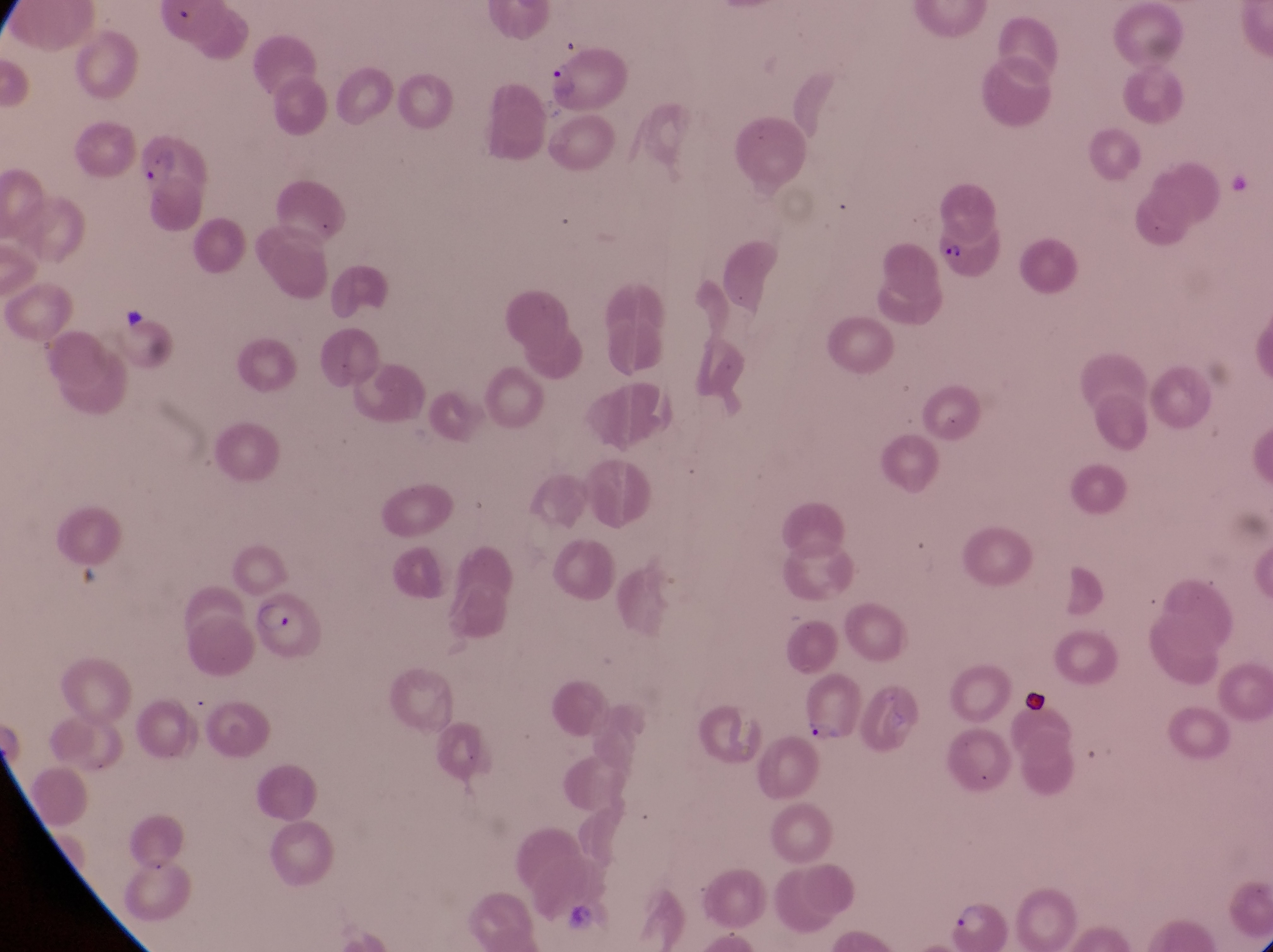
{
  "parasitised_red_blood_cell_locations": "approximate bounding boxes as (left, top, right, bottom) in pixels: (547, 48, 634, 116), (130, 130, 210, 188), (929, 225, 1009, 285), (250, 591, 327, 658), (799, 669, 861, 746), (941, 902, 1019, 949)",
  "image_size": "1273×952 pixels",
  "leukocyte_locations": "approximate bounding boxes as (left, top, right, bottom) in pixels: (1023, 682, 1053, 721)",
  "preparation": "thin blood film",
  "capture": "smartphone photograph through the eyepiece of an Olympus CX-23 microscope",
  "country": "Uganda",
  "field_of_view": "single",
  "magnification": "1000x"
}